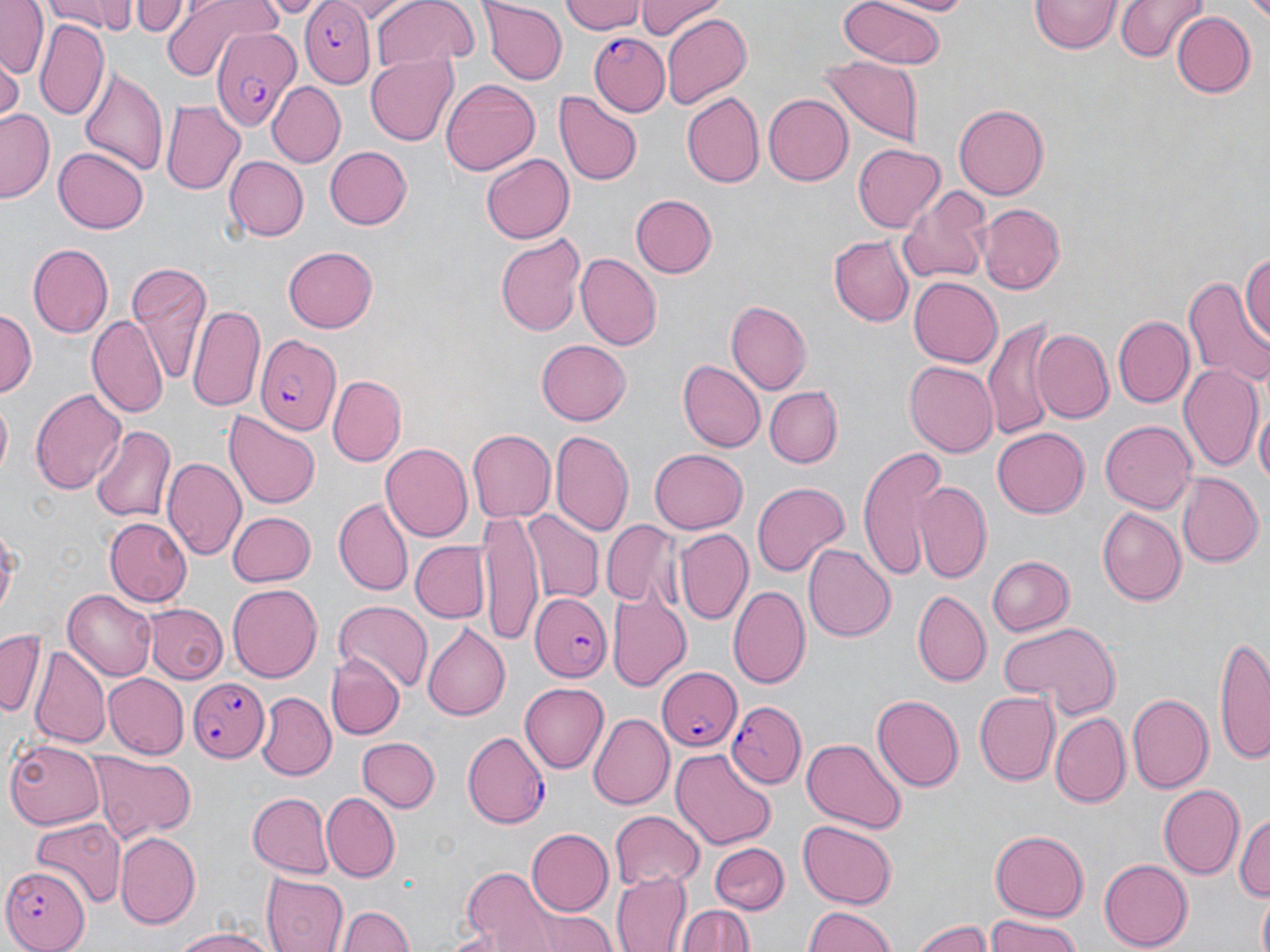 Approximate bounding boxes as named x1/y1/x2/y2 corners in pixels. Uninfected red blood cell locations: (x1=0, y1=0, x2=48, y2=78), (x1=44, y1=0, x2=137, y2=35), (x1=130, y1=0, x2=187, y2=37), (x1=158, y1=0, x2=283, y2=80), (x1=330, y1=0, x2=416, y2=20), (x1=371, y1=0, x2=475, y2=72), (x1=563, y1=0, x2=645, y2=36), (x1=633, y1=0, x2=724, y2=41), (x1=838, y1=0, x2=948, y2=72), (x1=878, y1=0, x2=979, y2=16), (x1=1115, y1=0, x2=1206, y2=64), (x1=481, y1=1, x2=566, y2=84), (x1=1030, y1=1, x2=1120, y2=56), (x1=1171, y1=11, x2=1256, y2=98), (x1=659, y1=13, x2=751, y2=110), (x1=36, y1=21, x2=110, y2=122), (x1=365, y1=54, x2=457, y2=146), (x1=0, y1=57, x2=21, y2=122), (x1=821, y1=57, x2=926, y2=145), (x1=78, y1=63, x2=167, y2=178), (x1=441, y1=79, x2=540, y2=175), (x1=267, y1=81, x2=346, y2=166), (x1=553, y1=92, x2=642, y2=186), (x1=680, y1=92, x2=765, y2=189), (x1=762, y1=94, x2=852, y2=185), (x1=162, y1=100, x2=244, y2=195), (x1=955, y1=104, x2=1050, y2=200), (x1=1, y1=109, x2=56, y2=203), (x1=851, y1=143, x2=944, y2=234), (x1=325, y1=146, x2=412, y2=230), (x1=54, y1=147, x2=148, y2=235), (x1=482, y1=153, x2=573, y2=244), (x1=224, y1=156, x2=307, y2=242), (x1=896, y1=185, x2=992, y2=285), (x1=629, y1=193, x2=718, y2=279), (x1=978, y1=202, x2=1066, y2=295), (x1=495, y1=230, x2=585, y2=337), (x1=830, y1=235, x2=914, y2=326), (x1=28, y1=243, x2=114, y2=336), (x1=283, y1=247, x2=377, y2=334), (x1=1241, y1=248, x2=1270, y2=348), (x1=575, y1=252, x2=662, y2=350), (x1=125, y1=263, x2=211, y2=383), (x1=909, y1=276, x2=1002, y2=369), (x1=1182, y1=276, x2=1270, y2=391), (x1=725, y1=301, x2=811, y2=395), (x1=188, y1=304, x2=264, y2=412), (x1=0, y1=308, x2=37, y2=399), (x1=1112, y1=314, x2=1193, y2=409), (x1=87, y1=317, x2=167, y2=418), (x1=983, y1=322, x2=1058, y2=441), (x1=1031, y1=330, x2=1114, y2=425), (x1=537, y1=341, x2=630, y2=426), (x1=677, y1=360, x2=764, y2=454), (x1=903, y1=361, x2=999, y2=457), (x1=1179, y1=363, x2=1264, y2=474), (x1=330, y1=375, x2=406, y2=466), (x1=764, y1=385, x2=841, y2=465), (x1=31, y1=386, x2=127, y2=496), (x1=0, y1=398, x2=11, y2=484), (x1=1254, y1=403, x2=1269, y2=498), (x1=222, y1=408, x2=322, y2=510), (x1=1101, y1=420, x2=1196, y2=513), (x1=91, y1=424, x2=176, y2=524), (x1=992, y1=426, x2=1088, y2=516), (x1=551, y1=429, x2=635, y2=541), (x1=467, y1=430, x2=554, y2=521), (x1=380, y1=444, x2=474, y2=541), (x1=855, y1=446, x2=950, y2=580), (x1=648, y1=448, x2=749, y2=534), (x1=163, y1=457, x2=246, y2=562), (x1=1175, y1=474, x2=1261, y2=568), (x1=914, y1=480, x2=992, y2=582), (x1=751, y1=481, x2=849, y2=578), (x1=332, y1=498, x2=414, y2=597), (x1=1098, y1=507, x2=1186, y2=604), (x1=478, y1=509, x2=544, y2=643), (x1=228, y1=510, x2=316, y2=587), (x1=523, y1=511, x2=603, y2=603), (x1=104, y1=518, x2=193, y2=606), (x1=602, y1=520, x2=679, y2=607), (x1=673, y1=529, x2=754, y2=626), (x1=409, y1=540, x2=490, y2=624), (x1=803, y1=541, x2=895, y2=642), (x1=984, y1=555, x2=1074, y2=638), (x1=226, y1=583, x2=322, y2=682), (x1=729, y1=585, x2=811, y2=689), (x1=913, y1=590, x2=991, y2=685), (x1=63, y1=591, x2=156, y2=681), (x1=608, y1=593, x2=689, y2=690), (x1=333, y1=600, x2=434, y2=692), (x1=143, y1=604, x2=227, y2=684), (x1=996, y1=619, x2=1121, y2=717), (x1=423, y1=624, x2=510, y2=720), (x1=0, y1=631, x2=43, y2=716), (x1=1215, y1=638, x2=1269, y2=763), (x1=30, y1=647, x2=111, y2=748), (x1=329, y1=655, x2=404, y2=738), (x1=104, y1=674, x2=188, y2=758), (x1=518, y1=680, x2=608, y2=772), (x1=976, y1=691, x2=1061, y2=784), (x1=257, y1=692, x2=335, y2=777), (x1=1126, y1=692, x2=1213, y2=795), (x1=870, y1=693, x2=964, y2=791), (x1=588, y1=713, x2=671, y2=809), (x1=1049, y1=713, x2=1129, y2=807), (x1=358, y1=736, x2=439, y2=812), (x1=799, y1=738, x2=905, y2=834), (x1=5, y1=741, x2=106, y2=828), (x1=671, y1=747, x2=776, y2=848), (x1=88, y1=753, x2=196, y2=840), (x1=1157, y1=784, x2=1244, y2=880), (x1=248, y1=792, x2=334, y2=878), (x1=320, y1=792, x2=399, y2=881), (x1=1234, y1=809, x2=1270, y2=909), (x1=610, y1=810, x2=705, y2=888), (x1=30, y1=817, x2=125, y2=907), (x1=798, y1=821, x2=896, y2=907), (x1=526, y1=827, x2=614, y2=914), (x1=990, y1=830, x2=1090, y2=919), (x1=114, y1=831, x2=199, y2=928), (x1=710, y1=843, x2=789, y2=915), (x1=1098, y1=859, x2=1193, y2=950), (x1=463, y1=868, x2=563, y2=951), (x1=614, y1=871, x2=692, y2=952), (x1=262, y1=873, x2=349, y2=952), (x1=1254, y1=892, x2=1270, y2=952), (x1=338, y1=902, x2=412, y2=952), (x1=677, y1=905, x2=757, y2=952), (x1=802, y1=907, x2=899, y2=951), (x1=521, y1=908, x2=618, y2=952), (x1=984, y1=915, x2=1081, y2=952), (x1=911, y1=919, x2=991, y2=952), (x1=168, y1=922, x2=280, y2=952). Plasmodium falciparum-infected red blood cell locations: (x1=300, y1=1, x2=376, y2=86), (x1=210, y1=28, x2=299, y2=129), (x1=590, y1=34, x2=669, y2=116), (x1=253, y1=333, x2=341, y2=434), (x1=532, y1=595, x2=609, y2=682), (x1=659, y1=667, x2=743, y2=753), (x1=188, y1=677, x2=269, y2=763), (x1=726, y1=701, x2=807, y2=786), (x1=462, y1=731, x2=549, y2=828), (x1=0, y1=864, x2=91, y2=951). Slide-level diagnosis: Plasmodium falciparum. Single field of view. Thin blood smear. 1000x magnification. Optical microscopy. May-Grünwald-Giemsa stain. Image is 1270×952 pixels.